Name the parasite shown.
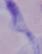
This is a trypanosome.

Photomicrograph. Captured at 1000x magnification.